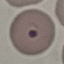
malaria status = parasitized
capture = smartphone camera at the microscope eyepiece
image type = cell patch, automatically extracted from a larger field of view and resized to 64 × 64 pixels
preparation = thin blood smear
stain = Giemsa